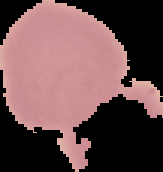
image type = cell region segmented out of the field of view; surrounding area masked to black
preparation = thin blood film
image size = 163×172 pixels
malaria status = uninfected